Locate every Plasmodium parasite.
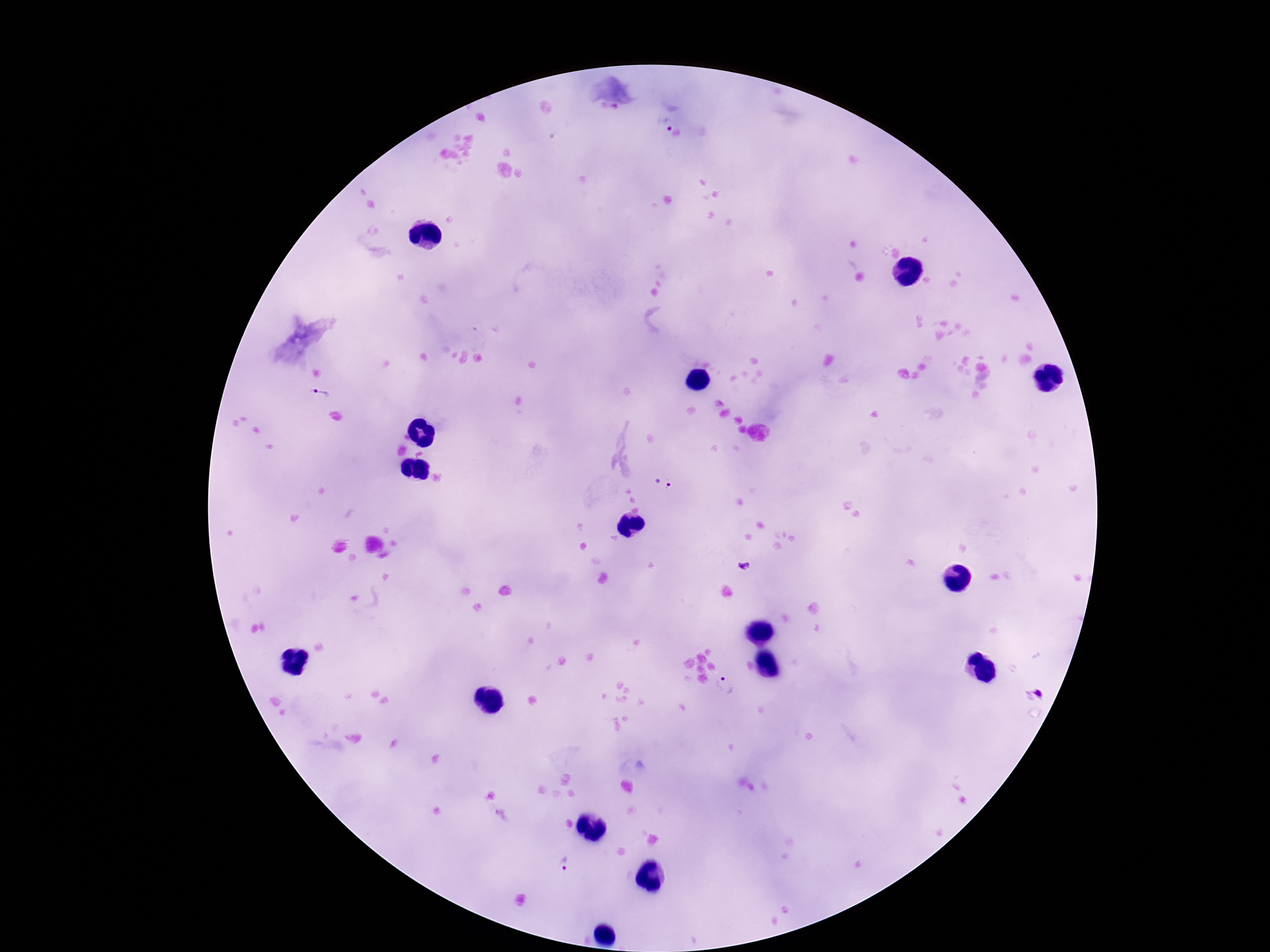
Approximate centers as (x, y) in pixels.
Plasmodium parasites: (608, 110), (666, 122), (319, 394), (663, 482), (744, 566), (727, 684), (1035, 692), (569, 862).

Thick blood film. 100x magnification. One field from this slide. Giemsa-stained preparation. Patient malaria status: infected. Image is 1270×952 pixels. Photographed through the microscope eyepiece with a smartphone camera.